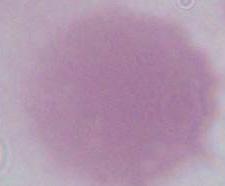
Summary:
  - Magnification: 1000x
  - Modality: photomicrograph
  - Identification: red blood cell